Locate every blood parasite and identify its species.
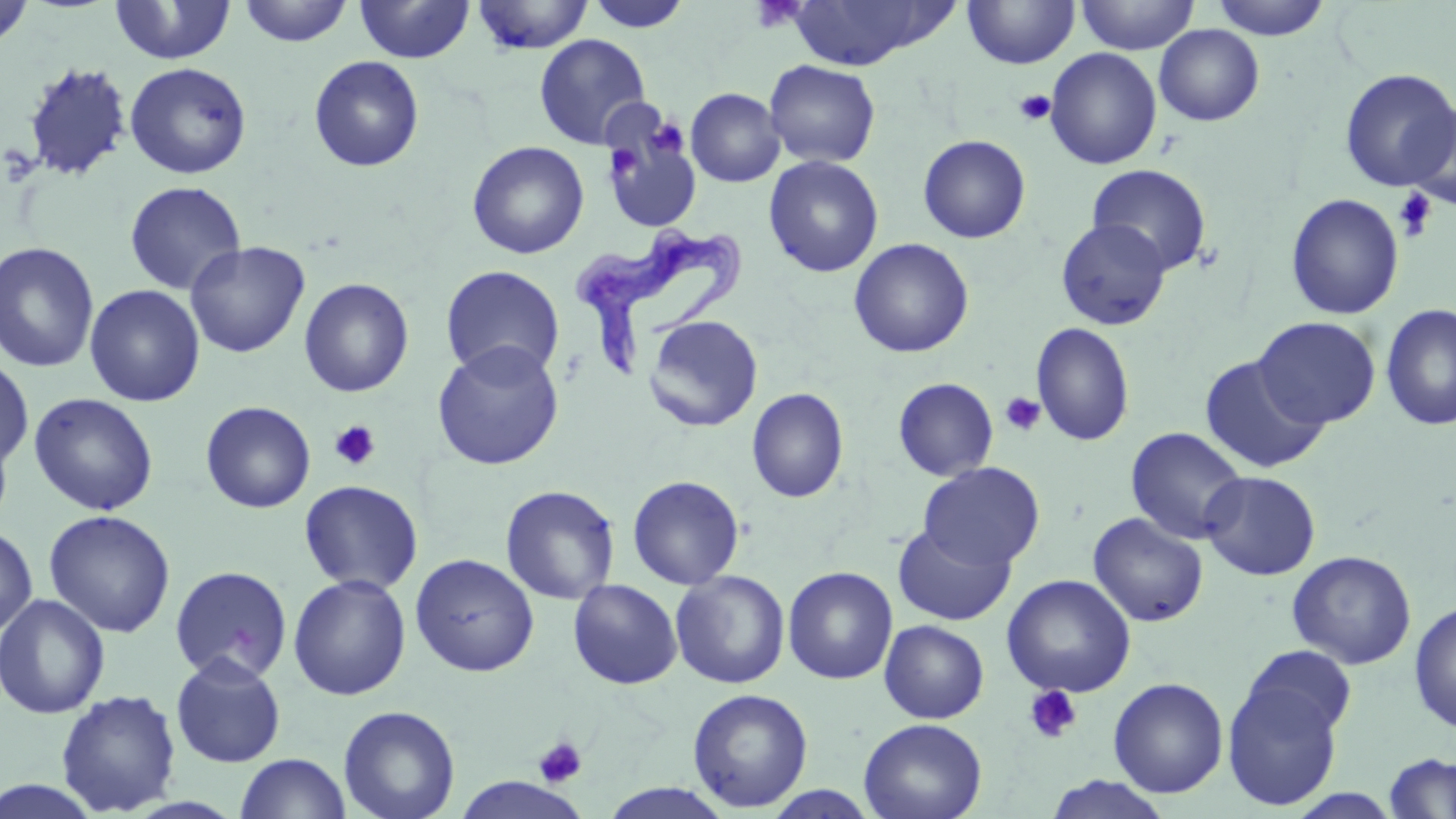
Approximate bounding boxes as (x1,y1)-(x2,y2) corner pairs in pixels.
Trypanosoma brucei: (568,222)-(742,373).
No Plasmodium falciparum, Plasmodium ovale, Plasmodium malariae, Plasmodium vivax, or Babesia divergens observed.

Platelet locations: (750,2)-(808,33), (1014,89)-(1056,126), (648,117)-(688,160), (606,145)-(642,181), (1394,188)-(1437,241), (1000,392)-(1046,437), (329,420)-(381,471), (1024,685)-(1082,743), (533,737)-(587,788). Uninfected red blood cell locations: (238,0)-(354,47), (356,0)-(474,63), (471,0)-(595,55), (584,0)-(693,33), (1075,0)-(1199,55), (1209,0)-(1333,40), (1,1)-(35,50), (109,1)-(237,65), (784,1)-(956,70), (962,1)-(1080,69), (1154,24)-(1265,126), (534,34)-(652,150), (1044,47)-(1163,170), (309,55)-(425,172), (764,59)-(881,168), (22,61)-(133,183), (124,62)-(252,179), (1339,68)-(1455,192), (686,88)-(785,187), (1406,102)-(1456,212), (604,131)-(693,227), (918,135)-(1031,243), (467,141)-(589,259), (764,155)-(884,278), (1087,164)-(1212,276), (124,180)-(246,295), (1285,193)-(1404,320), (1056,218)-(1172,330), (849,238)-(974,358), (0,241)-(100,373), (186,241)-(309,359), (441,265)-(565,381), (299,278)-(414,397), (84,284)-(205,407), (1380,303)-(1456,432), (643,315)-(763,433), (1254,316)-(1380,428), (1031,323)-(1135,446), (432,341)-(564,470), (1200,354)-(1330,475), (1,355)-(34,471), (893,378)-(998,480), (747,388)-(849,503), (28,392)-(159,516), (201,401)-(316,513), (0,421)-(14,534), (1125,426)-(1249,545), (918,461)-(1045,570), (1200,471)-(1321,580), (627,475)-(744,590), (299,479)-(423,594), (500,484)-(620,605), (43,510)-(176,637), (1088,512)-(1209,628), (892,522)-(1015,626), (0,525)-(38,638), (1287,551)-(1416,669), (410,553)-(539,677), (170,565)-(292,684), (783,566)-(898,685), (670,570)-(791,689), (288,574)-(411,701), (1001,574)-(1136,698), (567,579)-(683,690), (0,594)-(110,719), (1409,601)-(1456,734), (879,620)-(989,723), (1241,645)-(1357,742), (170,653)-(287,767), (1108,677)-(1228,798), (1223,679)-(1344,811), (687,688)-(813,812), (55,689)-(182,815), (338,705)-(460,819), (858,717)-(987,819), (1384,753)-(1456,818), (234,754)-(352,819), (1043,776)-(1173,819), (0,779)-(105,818), (600,783)-(735,818). Slide-level diagnosis: Trypanosoma brucei. May-Grünwald-Giemsa stain. Optical microscopy. 1000x magnification. Thin blood smear. One field of a larger specimen. Image is 1456×819 pixels.